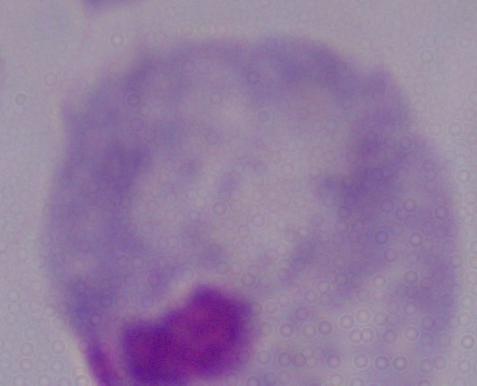

Summary:
  - Identification: trichomonad
  - Magnification: 1000x
  - Modality: micrograph